Report the malaria status of this cell.
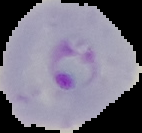

Parasitized.

Summary:
  - Image size: 142×133 pixels
  - Image type: segmented cell region with the area outside set to black
  - Preparation: thin blood film